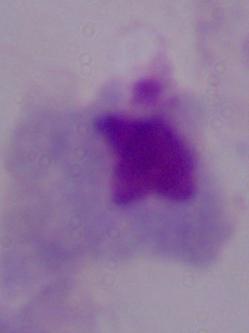

identification = trichomonad
modality = photomicrograph
magnification = 1000x